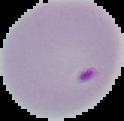
Summary:
  - Result: Plasmodium parasites detected
  - Image size: 124×121 pixels
  - Preparation: thin blood smear
  - Image type: segmented cell region with the area outside set to black